Identify the parasite.
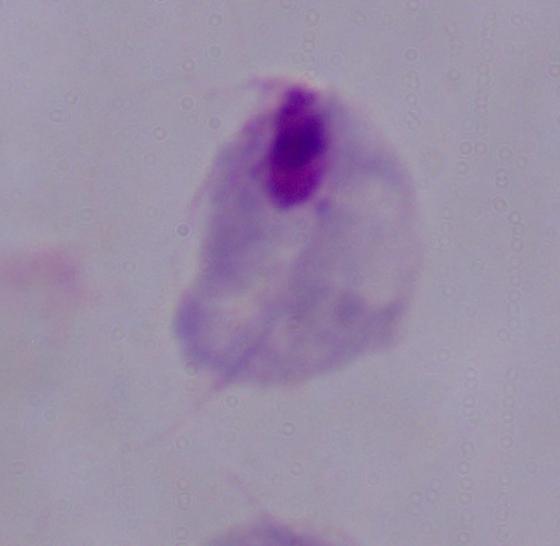

This is a trichomonad.

1000x magnification. Photomicrograph.